Point out Plasmodium parasites and leukocytes.
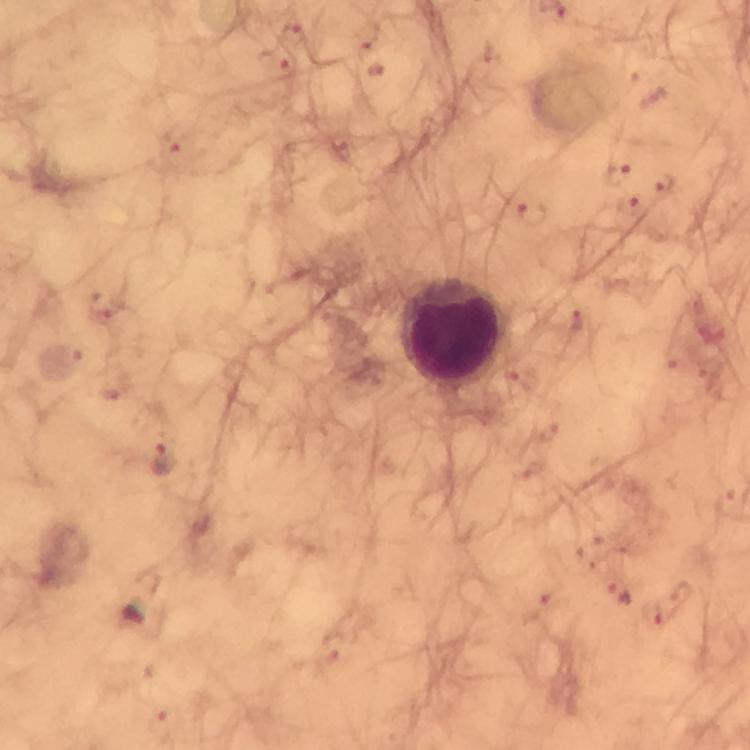
Approximate centers as [x, y] in pixels.
Plasmodium parasites: [616, 174], [667, 184], [630, 204], [532, 215], [164, 457].
Leukocytes: [458, 333].

Summary:
  - Cropped from: one field of view
  - Immersion oil: applied
  - Capture: smartphone mounted on the microscope
  - Image size: 750×750 pixels
  - Magnification: 100x
  - Preparation: thick blood smear
  - Context: from a malaria diagnostic workup
  - Stain: Giemsa